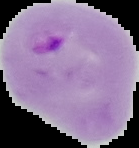
preparation = thin blood smear
malaria status = parasitized
image type = segmented cell region on a black background
image size = 139×148 pixels